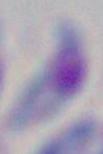
Summary:
  - Magnification: 1000x
  - Modality: micrograph
  - Identification: Toxoplasma gondii